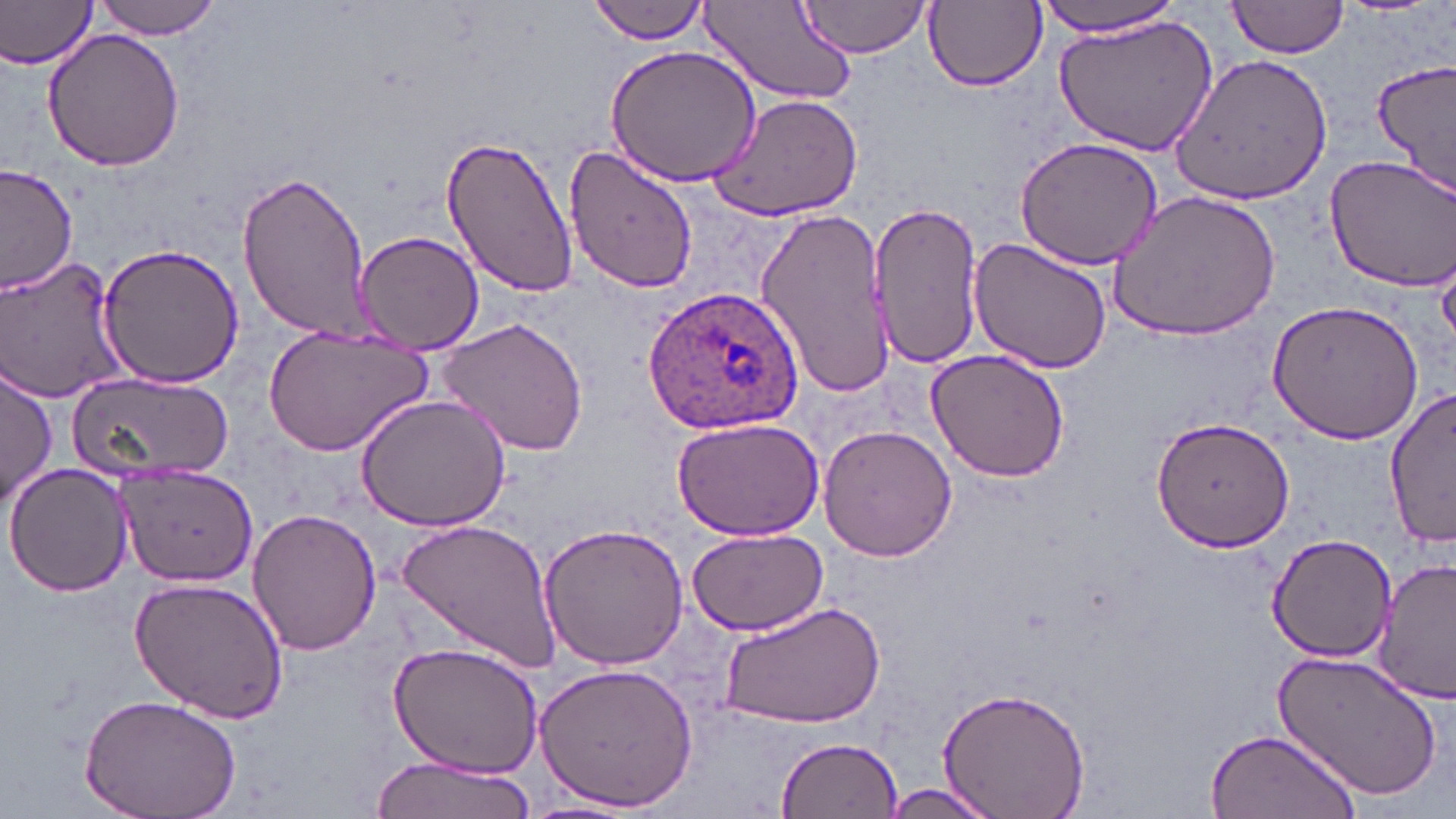

Approximate bounding boxes as named x1/y1/x2/y2 corners in pixels. Plasmodium ovale-infected red blood cell locations: (x1=642, y1=286, x2=805, y2=436). Uninfected red blood cell locations: (x1=0, y1=0, x2=100, y2=70), (x1=93, y1=0, x2=221, y2=40), (x1=797, y1=0, x2=931, y2=58), (x1=1035, y1=0, x2=1188, y2=37), (x1=1226, y1=0, x2=1349, y2=60), (x1=590, y1=1, x2=711, y2=42), (x1=920, y1=1, x2=1048, y2=94), (x1=699, y1=2, x2=859, y2=109), (x1=1052, y1=14, x2=1220, y2=156), (x1=41, y1=29, x2=187, y2=172), (x1=604, y1=45, x2=761, y2=188), (x1=1168, y1=51, x2=1333, y2=203), (x1=1372, y1=60, x2=1456, y2=193), (x1=707, y1=91, x2=864, y2=222), (x1=440, y1=133, x2=580, y2=298), (x1=1015, y1=135, x2=1166, y2=270), (x1=561, y1=140, x2=699, y2=294), (x1=1324, y1=155, x2=1456, y2=290), (x1=0, y1=165, x2=76, y2=298), (x1=235, y1=170, x2=373, y2=341), (x1=1107, y1=190, x2=1282, y2=342), (x1=870, y1=200, x2=984, y2=371), (x1=753, y1=204, x2=894, y2=402), (x1=355, y1=229, x2=485, y2=354), (x1=969, y1=239, x2=1114, y2=375), (x1=98, y1=242, x2=244, y2=389), (x1=1, y1=255, x2=128, y2=402), (x1=1266, y1=302, x2=1426, y2=445), (x1=438, y1=317, x2=591, y2=458), (x1=263, y1=325, x2=433, y2=454), (x1=924, y1=350, x2=1071, y2=483), (x1=1, y1=365, x2=56, y2=507), (x1=68, y1=370, x2=232, y2=482), (x1=1386, y1=387, x2=1455, y2=549), (x1=355, y1=393, x2=512, y2=532), (x1=1151, y1=416, x2=1296, y2=551), (x1=669, y1=417, x2=826, y2=539), (x1=817, y1=424, x2=957, y2=562), (x1=6, y1=461, x2=133, y2=599), (x1=117, y1=464, x2=258, y2=586), (x1=246, y1=508, x2=383, y2=656), (x1=398, y1=517, x2=560, y2=673), (x1=538, y1=522, x2=691, y2=672), (x1=685, y1=527, x2=828, y2=636), (x1=1266, y1=532, x2=1400, y2=662), (x1=1374, y1=558, x2=1456, y2=702), (x1=128, y1=576, x2=290, y2=725), (x1=718, y1=599, x2=887, y2=731), (x1=388, y1=641, x2=546, y2=779), (x1=1272, y1=646, x2=1444, y2=802), (x1=532, y1=663, x2=698, y2=812), (x1=935, y1=685, x2=1093, y2=819), (x1=78, y1=692, x2=244, y2=819), (x1=1204, y1=726, x2=1359, y2=819), (x1=776, y1=738, x2=903, y2=818), (x1=369, y1=754, x2=538, y2=819), (x1=871, y1=782, x2=1005, y2=819), (x1=520, y1=796, x2=648, y2=819). Slide-level diagnosis: Plasmodium ovale. Image is 1456×819 pixels. Thin blood film. Light microscopy. May-Grünwald-Giemsa-stained preparation. Captured at 1000x magnification. One field of a larger specimen.